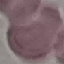

Summary:
  - Result: no malaria parasites seen
  - Capture: smartphone camera at the microscope eyepiece
  - Image type: cell patch, automatically extracted from a larger field of view and resized to 64 × 64 pixels
  - Preparation: thin smear
  - Stain: Giemsa